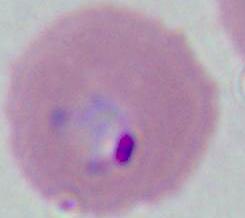

400x or 1000x magnification. A Plasmodium parasite is seen. Photomicrograph.